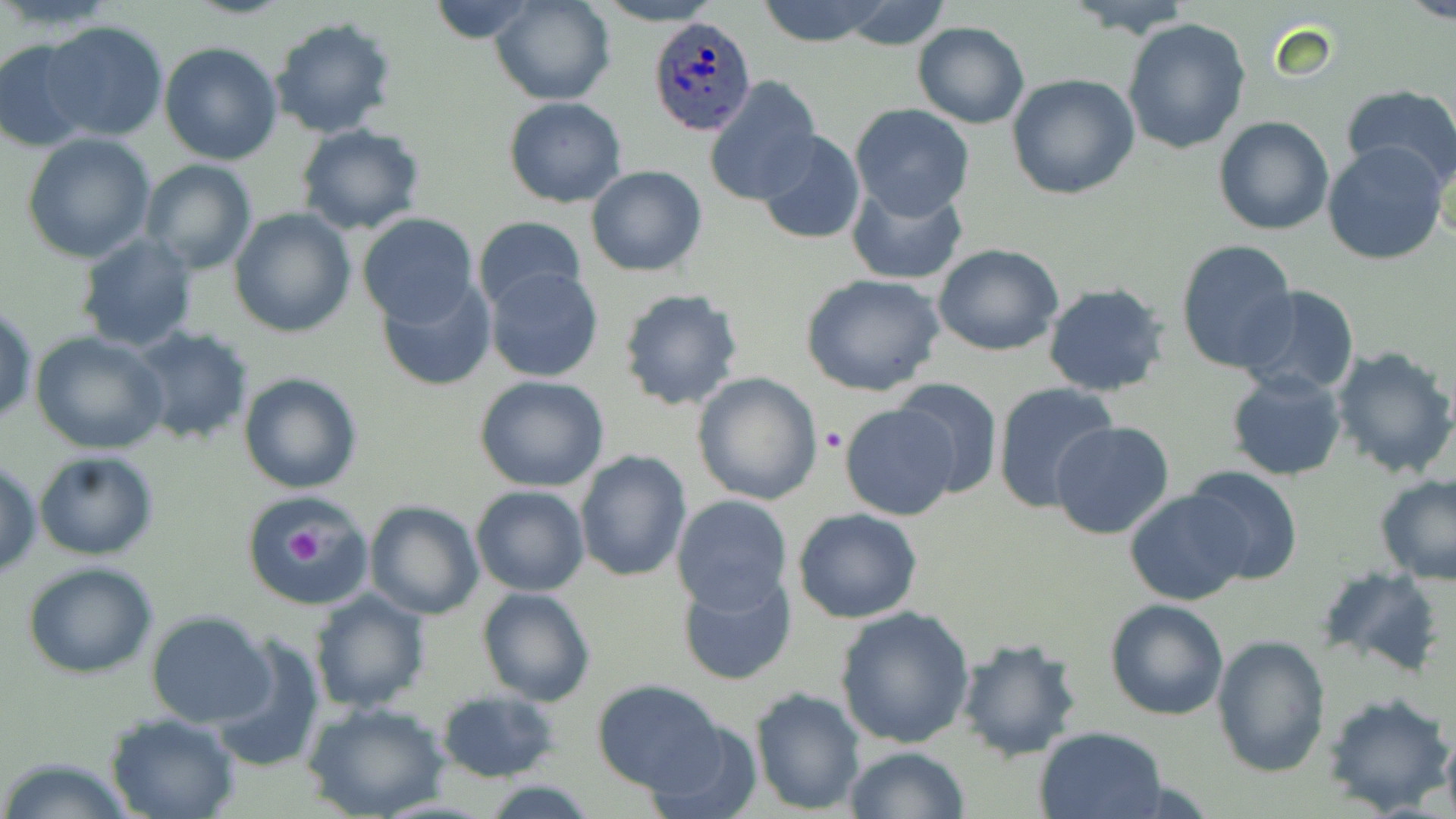

Approximate bounding boxes as (x1,y1)-(x2,y2) corner pairs in pixels. Platelet locations: (819,425)-(846,453), (280,521)-(326,570). Plasmodium ovale-infected red blood cell locations: (649,16)-(756,136). Uninfected red blood cell locations: (492,0)-(615,105), (592,0)-(722,26), (755,0)-(893,48), (1063,0)-(1200,37), (1402,0)-(1456,25), (829,1)-(957,51), (425,2)-(540,44), (271,15)-(398,138), (1121,18)-(1251,155), (40,19)-(171,142), (912,21)-(1029,129), (0,39)-(95,151), (159,41)-(284,165), (1006,72)-(1140,200), (703,76)-(820,206), (1339,85)-(1456,191), (502,97)-(627,208), (850,104)-(975,220), (1213,116)-(1335,235), (296,125)-(424,236), (755,130)-(866,245), (23,132)-(157,263), (1321,140)-(1451,267), (264,159)-(390,307), (139,161)-(257,274), (585,164)-(707,278), (845,176)-(968,285), (229,207)-(357,338), (357,213)-(480,328), (472,216)-(587,314), (74,232)-(197,354), (1173,239)-(1299,375), (932,243)-(1064,357), (484,266)-(603,382), (800,271)-(946,396), (375,276)-(495,392), (1041,281)-(1172,396), (1236,286)-(1363,400), (616,287)-(743,412), (1,303)-(37,427), (129,326)-(253,446), (29,330)-(170,456), (1331,345)-(1456,481), (1226,370)-(1348,481), (691,371)-(822,506), (238,372)-(363,493), (474,375)-(610,493), (890,377)-(1005,499), (991,383)-(1120,516), (838,401)-(964,521), (1049,420)-(1174,541), (573,449)-(692,582), (34,451)-(157,560), (0,460)-(43,580), (1184,464)-(1304,585), (1374,472)-(1456,585), (470,485)-(590,596), (1124,490)-(1251,606), (670,493)-(792,612), (243,497)-(372,610), (364,500)-(484,620), (793,509)-(923,623), (23,562)-(158,679), (1319,565)-(1445,676), (677,571)-(799,685), (477,587)-(596,707), (309,589)-(432,713), (1104,598)-(1231,720), (834,606)-(976,750), (146,611)-(275,726), (211,632)-(325,773), (1210,634)-(1329,777), (954,636)-(1083,762), (590,679)-(728,794), (749,687)-(865,814), (436,689)-(559,781), (1322,690)-(1452,814), (305,703)-(449,819), (105,713)-(240,819), (643,716)-(765,819), (1035,726)-(1168,819), (1439,726)-(1456,819), (841,746)-(969,819), (0,757)-(135,818). Slide-level diagnosis: Plasmodium ovale. Image is 1456×819 pixels. 1000x magnification. May-Grünwald-Giemsa stain. Thin blood smear. Optical microscopy. Single field of view.